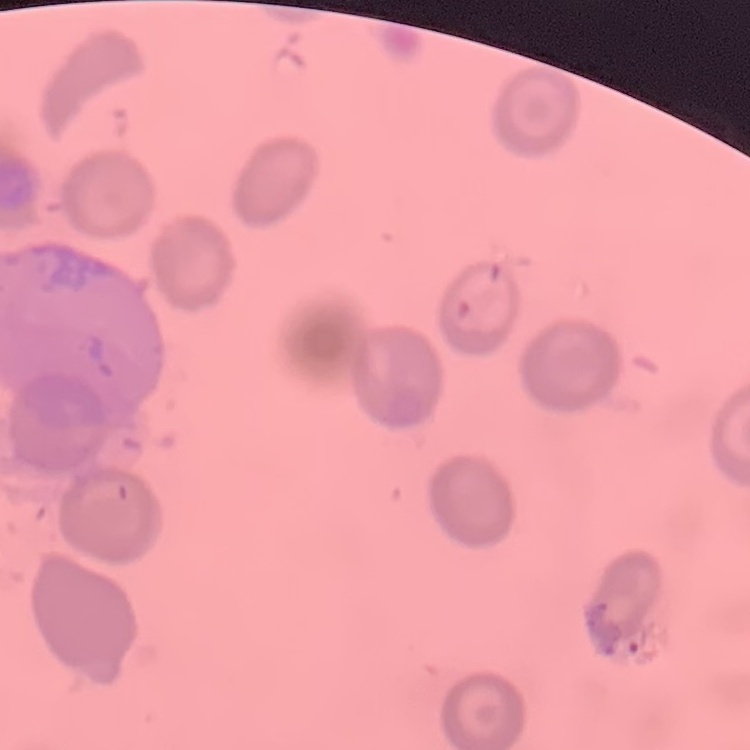

Summary:
  - Red blood cell morphology: no rouleaux formation
  - Preparation: thin blood smear
  - Image type: one tile cut from a larger photomicrograph
  - Stain: Field's or Giemsa